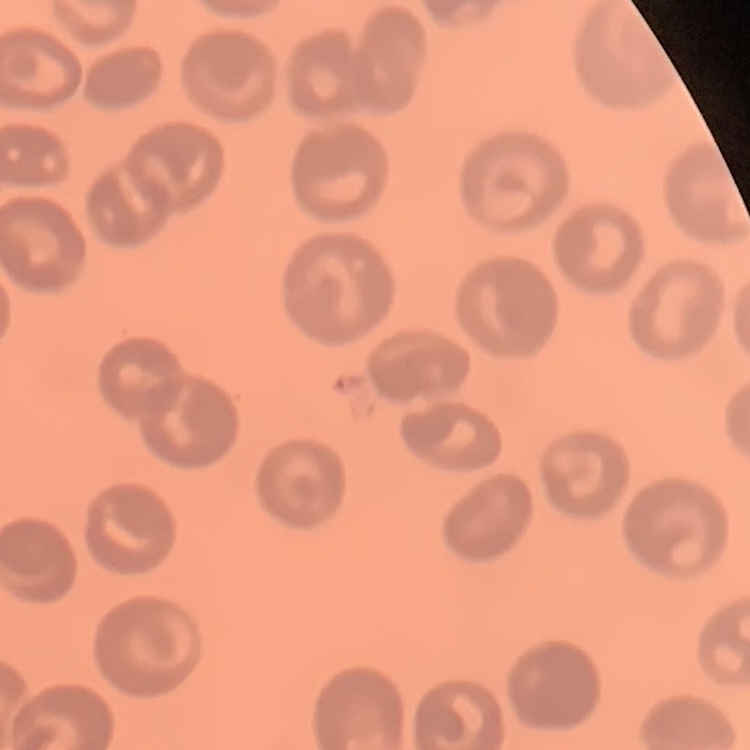

red blood cell morphology = no rouleaux formation
stain = Field's or Giemsa
image type = square crop of a larger photomicrograph
preparation = thin blood smear